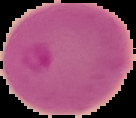

From a thin blood film. Result: Plasmodium parasites detected. Segmented cell region on a black background. Image is 136×118 pixels.